Identify the parasite.
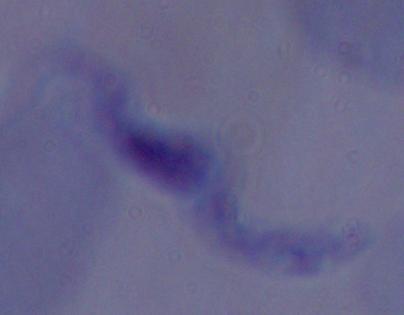
This is a trypanosome.

Summary:
  - Modality: micrograph
  - Magnification: 1000x